Report the malaria status of this cell.
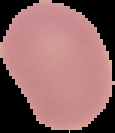

Uninfected.

{
  "image_size": "115×133 pixels",
  "preparation": "thin blood smear",
  "image_type": "segmented cell region with the area outside set to black"
}